Give the position of every Plasmodium parasite and every leukocyte.
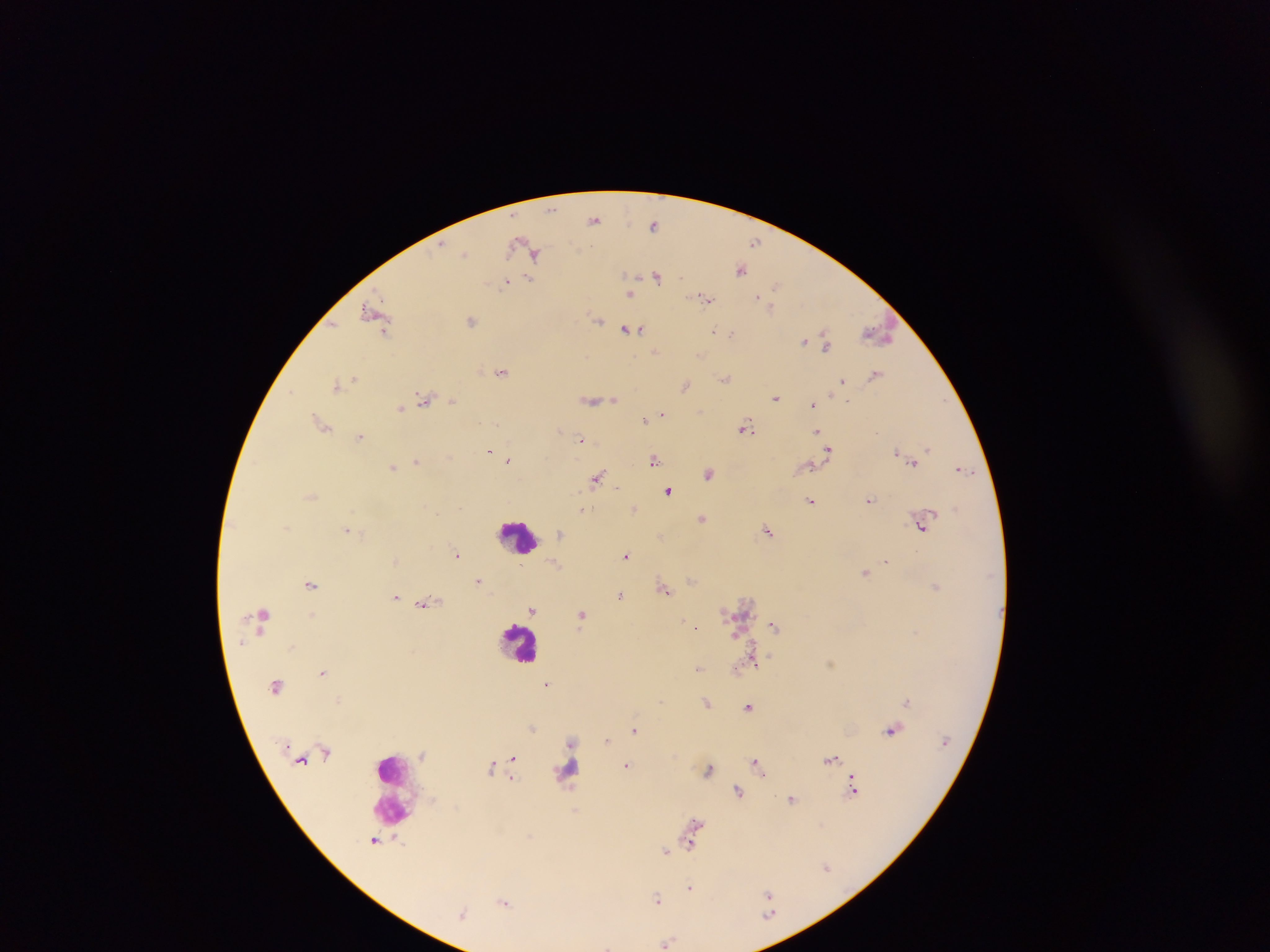
Approximate centers as {x, y} in pixels.
Plasmodium parasites: {595, 219}, {655, 224}, {755, 242}, {528, 247}, {465, 254}, {741, 269}, {657, 276}, {529, 280}, {507, 282}, {776, 286}, {629, 292}, {704, 297}, {771, 304}, {376, 314}, {598, 319}, {471, 320}, {629, 329}, {714, 331}, {732, 333}, {879, 333}, {806, 341}, {826, 342}, {656, 351}, {701, 353}, {502, 371}, {876, 375}, {355, 378}, {726, 378}, {844, 380}, {338, 383}, {685, 384}, {290, 391}, {776, 397}, {425, 399}, {591, 399}, {614, 399}, {452, 400}, {814, 404}, {400, 407}, {662, 413}, {646, 420}, {321, 422}, {745, 426}, {818, 431}, {361, 436}, {582, 440}, {928, 448}, {490, 449}, {829, 449}, {827, 453}, {900, 454}, {509, 460}, {654, 460}, {913, 460}, {417, 461}, {808, 465}, {393, 467}, {962, 468}, {710, 472}, {597, 479}, {669, 490}, {311, 496}, {811, 500}, {870, 500}, {634, 507}, {583, 509}, {702, 517}, {922, 524}, {288, 527}, {347, 529}, {768, 530}, {562, 532}, {661, 535}, {457, 555}, {625, 555}, {396, 560}, {886, 560}, {556, 564}, {866, 572}, {692, 580}, {480, 581}, {311, 583}, {664, 588}, {621, 594}, {396, 597}, {425, 602}, {533, 610}, {312, 614}, {582, 614}, {774, 625}, {695, 626}, {736, 634}, {755, 661}, {831, 662}, {700, 668}, {735, 669}, {323, 672}, {547, 684}, {339, 700}, {908, 701}, {708, 702}, {749, 706}, {533, 728}, {635, 729}, {893, 729}, {607, 739}, {572, 741}, {424, 755}, {513, 757}, {831, 758}, {757, 762}, {627, 765}, {493, 767}, {710, 769}, {512, 776}, {855, 790}, {738, 791}, {793, 798}, {575, 810}, {695, 824}, {692, 834}, {530, 836}, {691, 842}, {667, 851}, {827, 867}, {690, 887}, {768, 895}, {657, 899}, {505, 900}, {463, 913}, {667, 941}.
Leukocytes: {520, 535}, {520, 642}, {569, 772}, {393, 789}.

Photographed through a microscope with a mobile-phone camera. Image is 1270×952 pixels. Thick blood smear. One field of view. Sample from Ghana.